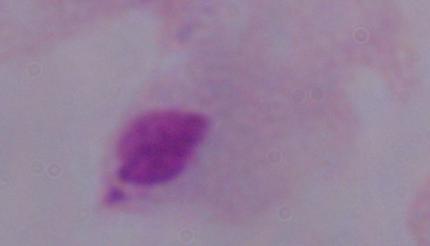
magnification = 1000x
modality = micrograph
identification = trichomonad